Point out every malaria parasite and every leukocyte.
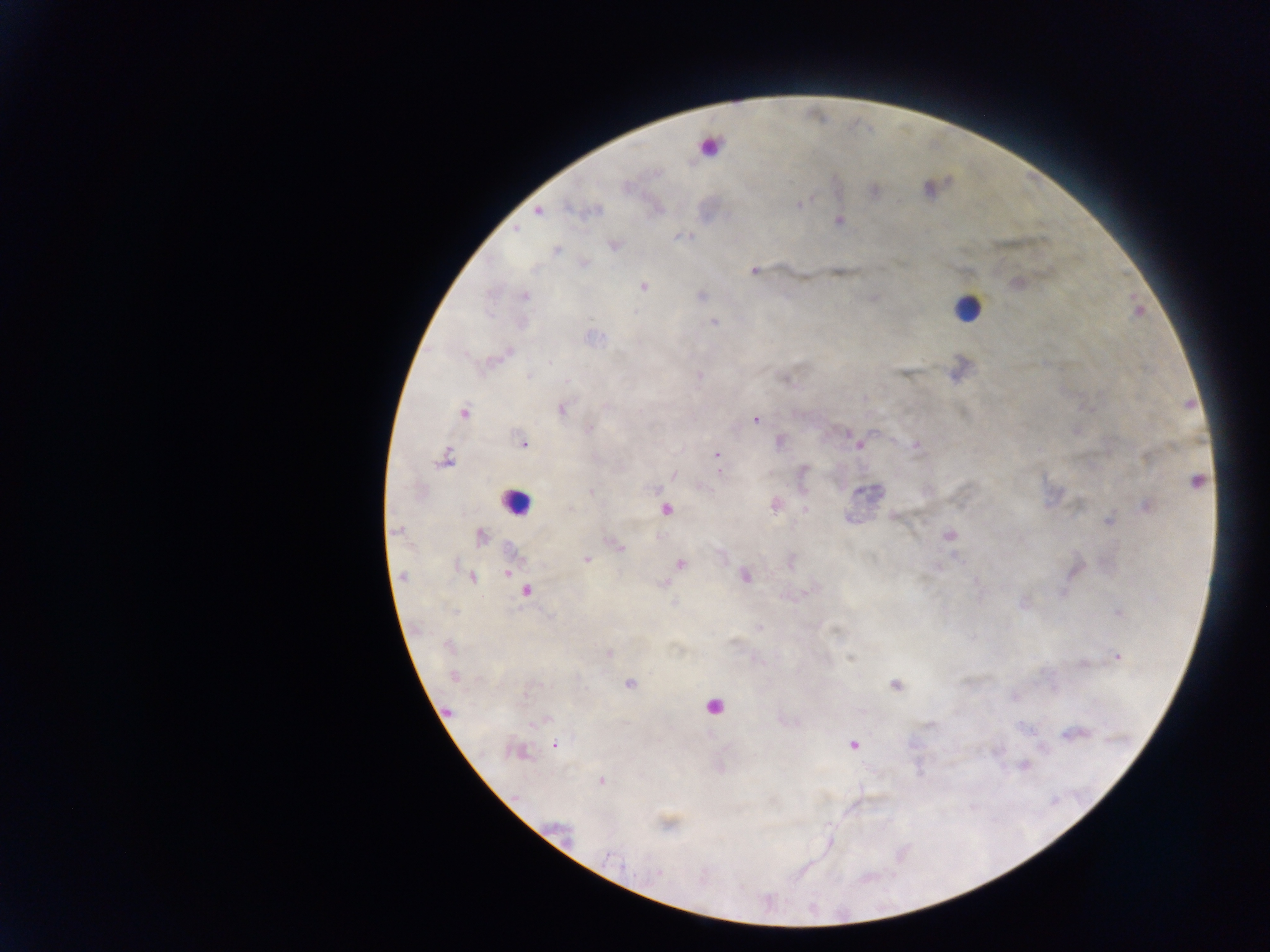

Approximate centers as x y in pixels.
Malaria parasites: 626 186; 799 205; 596 210; 538 212; 839 221; 515 229; 614 245; 557 251; 585 263; 755 270; 643 287; 525 296; 714 322; 549 363; 699 375; 529 377; 567 380; 605 405; 562 409; 463 412; 755 419; 588 429; 523 444; 859 445; 916 445; 717 454; 446 457; 804 469; 720 472; 674 474; 1195 482; 591 492; 1147 506; 570 508; 806 509; 666 510; 1108 521; 395 529; 948 534; 480 536; 614 544; 619 547; 586 559; 680 563; 507 573; 745 576; 402 577; 473 577; 664 584; 527 591; 454 611; 1119 613; 759 628; 448 645; 609 653; 1117 656; 850 658; 454 676; 630 684; 895 685; 448 712; 541 721; 1071 735; 854 745; 555 746; 518 752; 1024 766; 601 780; 612 859; 658 873.
Leukocytes: 702 196; 967 309; 515 501; 713 706.

Summary:
  - Capture: mobile-phone photograph through a microscope
  - Preparation: thick blood film
  - Image size: 1270×952 pixels
  - Field of view: single
  - Country: Ghana